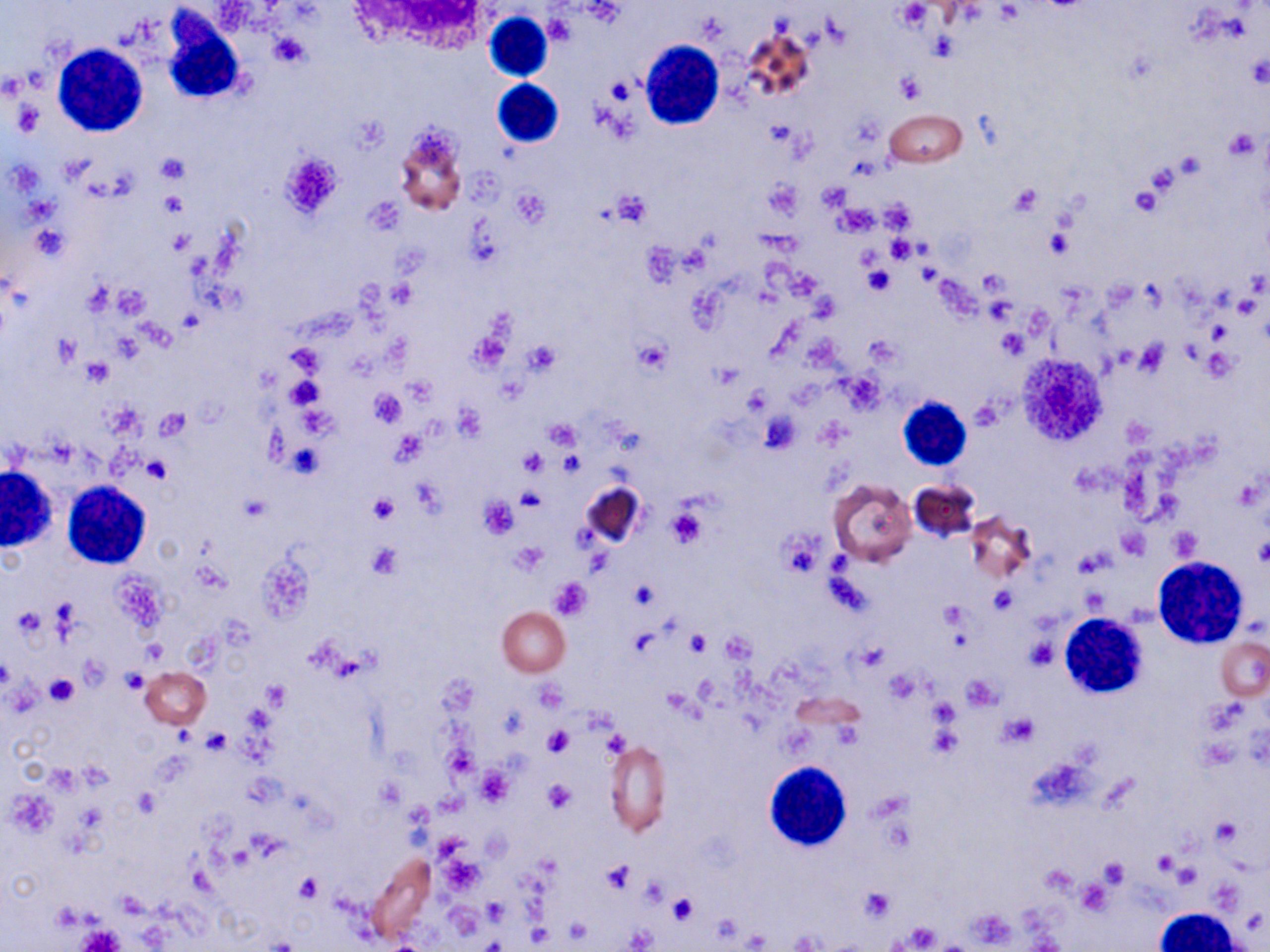
slide_level_diagnosis: negative for blood parasites
field_of_view: one of a larger specimen
magnification: 1000x
stain: May-Grünwald-Giemsa
image_size: 1270×952 pixels
uninfected_red_blood_cell_locations: 'approximate bounding boxes as (x1,y1)-(x2,y2) corner pairs in pixels: (740,23)-(815,105), (884,108)-(968,167), (393,124)-(467,213), (828,479)-(916,566), (909,479)-(982,544), (580,481)-(648,551), (965,511)-(1038,583), (497,607)-(571,677), (1216,636)-(1268,702), (140,667)-(211,729), (605,741)-(671,835), (369,851)-(436,944), (1155,908)-(1243,951)'
modality: optical microscopy
white_blood_cell_locations: 'approximate bounding boxes as (x1,y1)-(x2,y2) corner pairs in pixels: (484,11)-(555,82), (161,13)-(244,103), (639,39)-(723,130), (53,44)-(149,137), (492,79)-(564,148), (896,396)-(973,471), (0,468)-(55,550), (60,482)-(152,569), (1153,556)-(1248,647), (1065,615)-(1150,703), (765,761)-(852,851)'
preparation: thin blood smear
platelet_locations: 'approximate bounding boxes as (x1,y1)-(x2,y2) corner pairs in pixels: (898,2)-(932,27), (544,13)-(575,46), (271,33)-(309,67), (896,73)-(925,102), (608,78)-(636,103), (12,102)-(44,133), (1224,129)-(1260,164), (279,151)-(343,219), (155,154)-(191,184), (1142,160)-(1184,200), (764,178)-(803,218), (818,182)-(853,212), (1007,184)-(1043,217), (1130,184)-(1162,217), (511,190)-(547,227), (158,191)-(187,217), (609,192)-(652,227), (835,205)-(879,237), (33,226)-(68,261), (1045,228)-(1073,258), (167,229)-(192,255), (888,236)-(917,262), (864,265)-(893,295), (389,281)-(415,307), (983,297)-(1016,325), (469,328)-(513,372), (998,328)-(1029,359), (55,335)-(80,368), (633,337)-(671,376), (523,340)-(560,376), (1133,341)-(1171,379), (287,345)-(324,374), (1203,346)-(1237,382), (82,358)-(113,386), (287,376)-(323,410), (370,388)-(405,427), (154,411)-(189,438), (761,414)-(801,453), (544,418)-(580,449), (392,431)-(425,465), (521,449)-(548,476), (559,450)-(583,476), (143,456)-(171,483), (514,488)-(543,512), (368,494)-(398,524), (479,497)-(518,538), (667,509)-(707,549), (1168,526)-(1203,561), (778,527)-(827,580), (1254,536)-(1270,569), (365,542)-(403,579), (512,544)-(547,575), (549,579)-(593,619), (629,580)-(660,610), (989,588)-(1016,614), (685,632)-(710,657), (1026,638)-(1057,669), (120,669)-(149,694), (44,675)-(78,705), (263,682)-(287,709), (534,682)-(567,712), (1003,713)-(1037,745), (927,725)-(959,757), (541,727)-(573,758), (203,729)-(231,754), (445,747)-(478,781), (477,768)-(514,805), (545,780)-(574,813), (133,788)-(162,819), (1212,817)-(1240,846), (1099,859)-(1128,888), (600,860)-(636,893), (1172,862)-(1199,889), (296,873)-(322,901), (1077,880)-(1112,915), (859,887)-(894,921), (669,892)-(699,923), (75,926)-(125,952)'